Name the parasite shown.
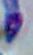

This is Toxoplasma gondii.

Photomicrograph. Captured at 1000x magnification.